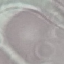

malaria status = uninfected
stain = Giemsa
image type = automatically extracted cell patch, resized to 64 × 64 pixels
capture = smartphone camera at the microscope eyepiece
preparation = thin blood smear